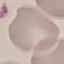
Summary:
  - Result: no malaria parasites detected
  - Capture: smartphone through the microscope eyepiece
  - Preparation: thin smear
  - Image type: cell patch, automatically extracted from a larger field of view and resized to 64 × 64 pixels
  - Stain: Giemsa